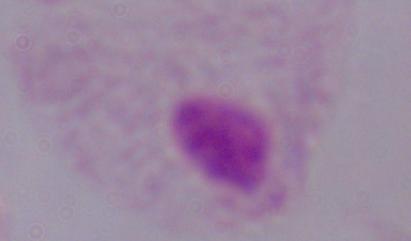

Summary:
  - Magnification: 1000x
  - Identification: trichomonad
  - Modality: photomicrograph